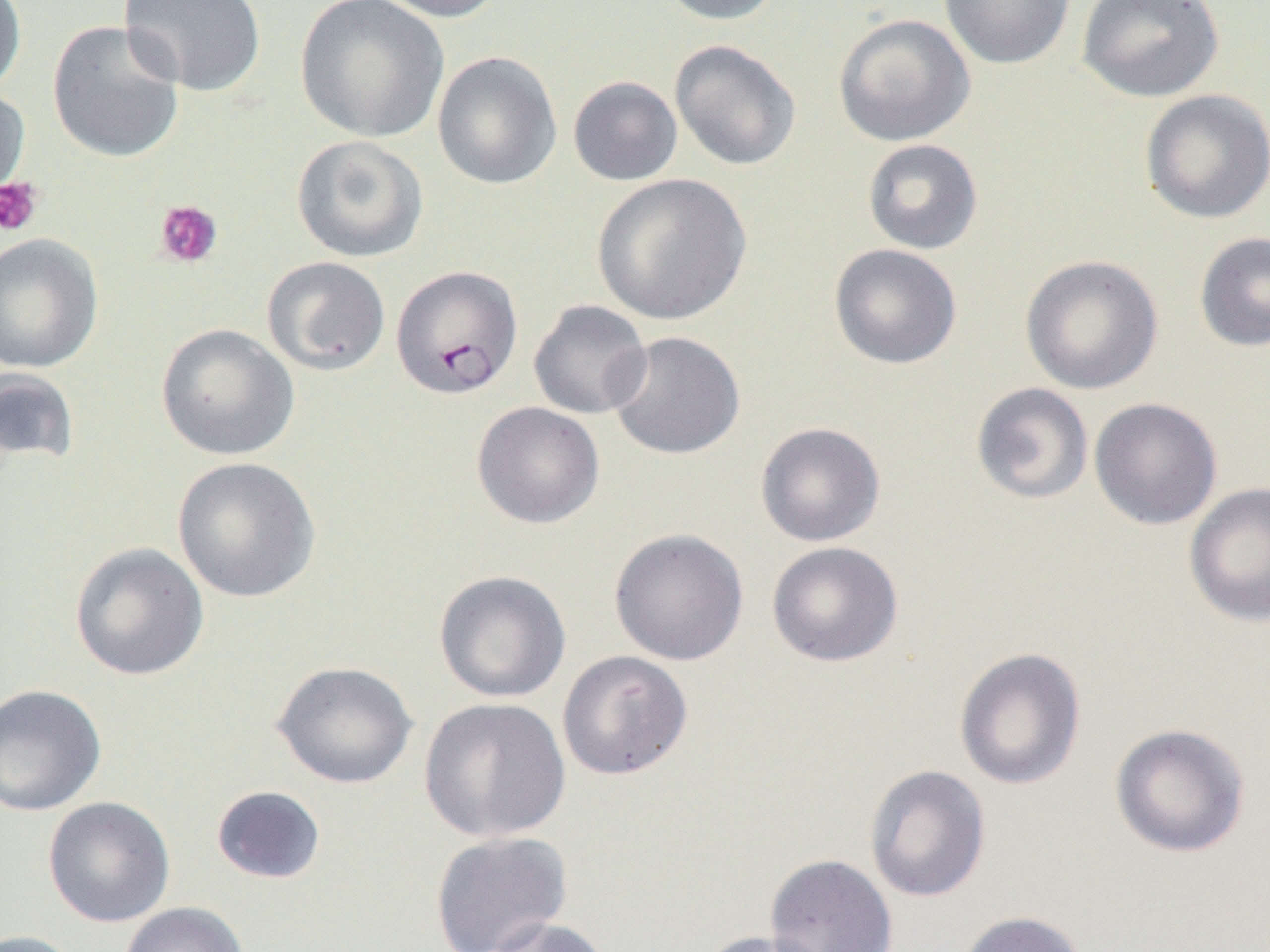

Summary:
  - Coordinate format: approximate bounding boxes as (x1, y1, x2, y2) in pixels
  - Uninfected red blood cell locations: (0, 0, 27, 98), (118, 0, 267, 97), (294, 0, 449, 143), (371, 0, 508, 23), (655, 0, 788, 25), (938, 0, 1075, 69), (1076, 0, 1225, 103), (833, 13, 975, 147), (47, 20, 185, 163), (669, 39, 801, 171), (432, 51, 562, 190), (568, 76, 683, 186), (0, 84, 31, 209), (1139, 89, 1270, 224), (290, 134, 429, 263), (862, 138, 984, 255), (591, 174, 752, 326), (1193, 231, 1270, 352), (0, 233, 103, 373), (829, 243, 963, 369), (1019, 254, 1164, 395), (262, 256, 391, 376), (528, 300, 652, 419), (155, 323, 299, 461), (606, 331, 745, 460), (0, 367, 81, 470), (970, 382, 1094, 505), (1089, 397, 1223, 530), (471, 401, 604, 529), (755, 422, 885, 547), (172, 457, 321, 603), (1184, 482, 1270, 627), (608, 528, 749, 666), (766, 541, 904, 668), (69, 542, 209, 681), (433, 569, 571, 703), (954, 647, 1086, 790), (557, 650, 693, 780), (271, 660, 419, 790), (0, 683, 107, 817), (419, 697, 571, 842), (1109, 722, 1251, 858), (863, 764, 991, 902), (210, 785, 327, 884), (42, 796, 175, 928), (429, 831, 573, 952), (765, 852, 898, 952), (119, 902, 249, 952), (955, 911, 1088, 952), (482, 916, 613, 952), (0, 929, 85, 952), (695, 930, 835, 952)
  - Plasmodium falciparum-infected red blood cell locations: (388, 264, 520, 399)
  - Platelet locations: (0, 176, 44, 236), (154, 199, 223, 268)
  - Slide-level diagnosis: Plasmodium falciparum
  - Magnification: 1000x
  - Field of view: single
  - Preparation: thin blood smear
  - Modality: light microscopy
  - Image size: 1270×952 pixels